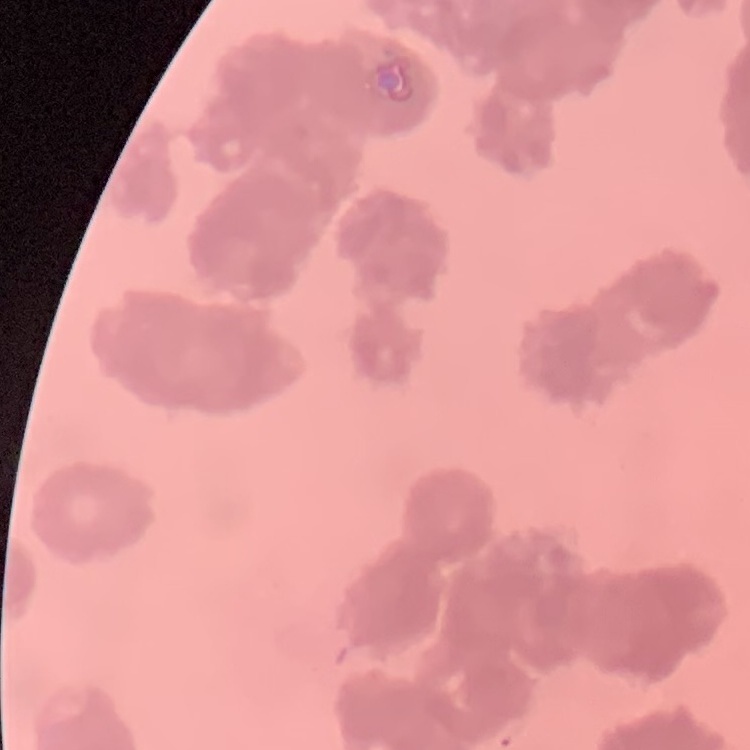
erythrocyte morphology = rouleaux formation
stain = Field's or Giemsa
image type = square crop of a larger photomicrograph
preparation = thin peripheral smear